State the blood parasite species.
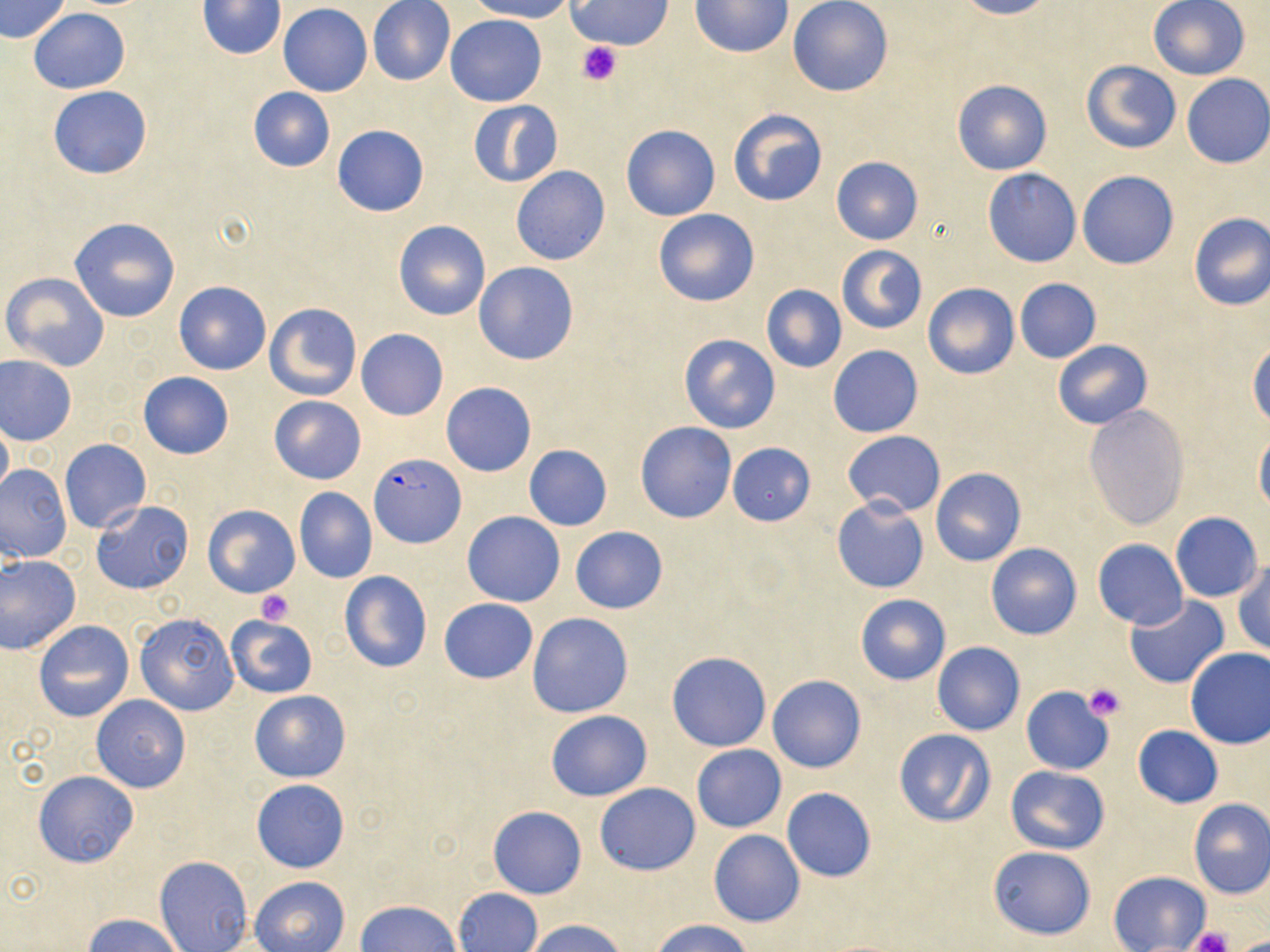
Plasmodium falciparum.

{
  "field_of_view": "single",
  "stain": "May-Grünwald-Giemsa",
  "modality": "light microscopy",
  "plasmodium_falciparum_infected_red_blood_cell_locations": "approximate bounding boxes as named x1/y1/x2/y2 corners in pixels: (x1=370, y1=453, x2=466, y2=549)",
  "platelet_locations": "approximate bounding boxes as named x1/y1/x2/y2 corners in pixels: (x1=577, y1=41, x2=620, y2=85), (x1=256, y1=589, x2=293, y2=626), (x1=1083, y1=683, x2=1126, y2=721), (x1=1190, y1=927, x2=1232, y2=952)",
  "preparation": "thin blood film",
  "magnification": "1000x",
  "uninfected_red_blood_cell_locations": "approximate bounding boxes as named x1/y1/x2/y2 corners in pixels: (x1=1, y1=0, x2=71, y2=43), (x1=367, y1=0, x2=456, y2=86), (x1=464, y1=0, x2=573, y2=22), (x1=567, y1=0, x2=673, y2=50), (x1=690, y1=0, x2=793, y2=58), (x1=788, y1=0, x2=894, y2=98), (x1=955, y1=0, x2=1056, y2=20), (x1=195, y1=1, x2=288, y2=58), (x1=1147, y1=1, x2=1250, y2=80), (x1=278, y1=4, x2=373, y2=96), (x1=28, y1=8, x2=131, y2=94), (x1=446, y1=14, x2=546, y2=106), (x1=1082, y1=60, x2=1180, y2=154), (x1=1181, y1=74, x2=1270, y2=169), (x1=952, y1=79, x2=1051, y2=175), (x1=47, y1=85, x2=153, y2=180), (x1=247, y1=87, x2=335, y2=173), (x1=467, y1=100, x2=563, y2=186), (x1=728, y1=109, x2=827, y2=207), (x1=621, y1=124, x2=720, y2=221), (x1=332, y1=125, x2=429, y2=217), (x1=831, y1=157, x2=923, y2=245), (x1=510, y1=166, x2=610, y2=266), (x1=982, y1=168, x2=1082, y2=267), (x1=1076, y1=171, x2=1179, y2=270), (x1=652, y1=208, x2=760, y2=307), (x1=1187, y1=212, x2=1270, y2=310), (x1=68, y1=217, x2=180, y2=323), (x1=393, y1=220, x2=490, y2=321), (x1=836, y1=245, x2=927, y2=334), (x1=473, y1=262, x2=579, y2=365), (x1=2, y1=272, x2=110, y2=371), (x1=1014, y1=278, x2=1101, y2=363), (x1=173, y1=280, x2=271, y2=375), (x1=923, y1=282, x2=1019, y2=379), (x1=762, y1=284, x2=847, y2=374), (x1=264, y1=301, x2=362, y2=402), (x1=356, y1=328, x2=448, y2=421), (x1=678, y1=333, x2=781, y2=434), (x1=1052, y1=339, x2=1152, y2=430), (x1=1248, y1=342, x2=1269, y2=431), (x1=828, y1=345, x2=923, y2=438), (x1=1, y1=355, x2=77, y2=444), (x1=138, y1=371, x2=235, y2=460), (x1=441, y1=382, x2=537, y2=477), (x1=268, y1=396, x2=367, y2=485), (x1=1083, y1=404, x2=1190, y2=530), (x1=1, y1=416, x2=12, y2=502), (x1=635, y1=422, x2=737, y2=523), (x1=1254, y1=430, x2=1270, y2=515), (x1=842, y1=431, x2=945, y2=516), (x1=60, y1=438, x2=151, y2=532), (x1=727, y1=442, x2=816, y2=526), (x1=523, y1=444, x2=612, y2=531), (x1=0, y1=463, x2=72, y2=564), (x1=930, y1=467, x2=1025, y2=565), (x1=294, y1=487, x2=377, y2=583), (x1=831, y1=497, x2=930, y2=594), (x1=91, y1=500, x2=193, y2=595), (x1=203, y1=505, x2=299, y2=597), (x1=462, y1=512, x2=565, y2=607), (x1=1169, y1=512, x2=1263, y2=601), (x1=570, y1=526, x2=668, y2=614), (x1=1092, y1=539, x2=1188, y2=629), (x1=985, y1=542, x2=1083, y2=639), (x1=0, y1=554, x2=82, y2=654), (x1=1233, y1=561, x2=1270, y2=656), (x1=339, y1=572, x2=431, y2=673), (x1=856, y1=594, x2=950, y2=685), (x1=1124, y1=596, x2=1230, y2=689), (x1=440, y1=598, x2=537, y2=684), (x1=133, y1=612, x2=238, y2=715), (x1=526, y1=612, x2=635, y2=718), (x1=226, y1=615, x2=318, y2=697), (x1=33, y1=620, x2=134, y2=722), (x1=932, y1=642, x2=1024, y2=736), (x1=1184, y1=647, x2=1270, y2=749), (x1=666, y1=651, x2=771, y2=751), (x1=767, y1=674, x2=866, y2=773), (x1=1020, y1=686, x2=1113, y2=775), (x1=249, y1=689, x2=351, y2=782), (x1=91, y1=694, x2=190, y2=793), (x1=545, y1=710, x2=652, y2=802), (x1=1133, y1=725, x2=1222, y2=808), (x1=894, y1=729, x2=997, y2=828), (x1=692, y1=745, x2=786, y2=832), (x1=1006, y1=766, x2=1110, y2=854), (x1=33, y1=770, x2=140, y2=867), (x1=251, y1=778, x2=349, y2=873), (x1=595, y1=783, x2=700, y2=875), (x1=782, y1=787, x2=876, y2=883), (x1=1187, y1=798, x2=1270, y2=899), (x1=487, y1=806, x2=586, y2=899), (x1=709, y1=830, x2=804, y2=928), (x1=988, y1=845, x2=1096, y2=940), (x1=155, y1=855, x2=252, y2=951), (x1=1109, y1=871, x2=1210, y2=952), (x1=250, y1=876, x2=349, y2=952), (x1=453, y1=889, x2=541, y2=952), (x1=357, y1=900, x2=460, y2=951), (x1=83, y1=914, x2=186, y2=952), (x1=524, y1=918, x2=630, y2=952), (x1=650, y1=919, x2=756, y2=952)",
  "image_size": "1270×952 pixels"
}